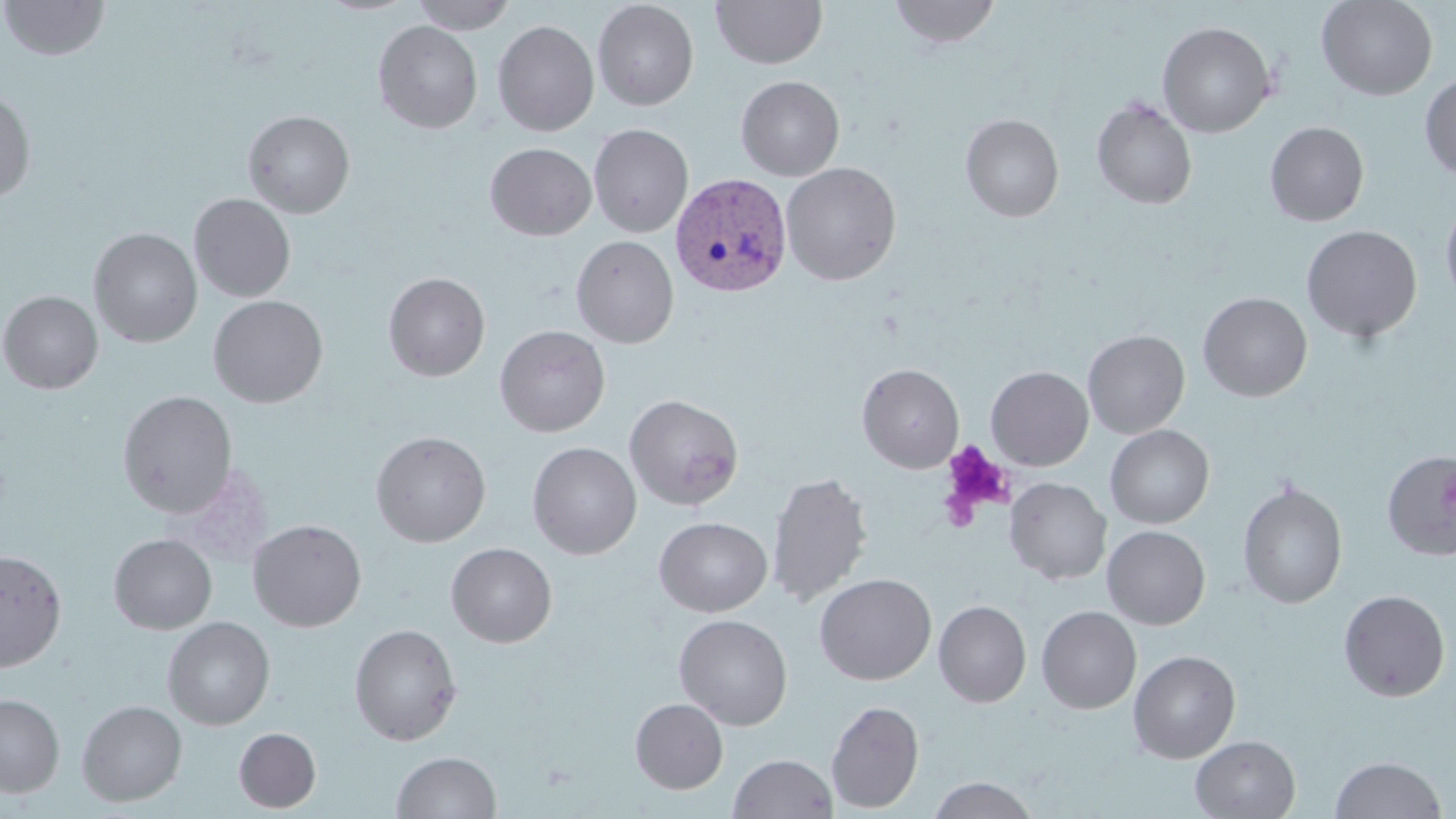
{
  "slide_level_diagnosis": "Plasmodium vivax",
  "magnification": "1000x",
  "uninfected_red_blood_cell_locations": "approximate bounding boxes as (x1,y1)-(x2,y2) corner pairs in pixels: (2,0)-(109,61), (409,0)-(517,34), (711,0)-(827,69), (888,0)-(1002,49), (1317,0)-(1437,100), (592,1)-(699,110), (492,20)-(599,136), (373,21)-(483,133), (1157,21)-(1275,137), (1419,73)-(1456,180), (736,75)-(845,181), (0,90)-(36,203), (1092,96)-(1197,210), (243,110)-(355,218), (960,113)-(1064,222), (1265,121)-(1369,226), (589,124)-(693,237), (485,142)-(597,241), (781,162)-(902,286), (189,193)-(296,302), (1440,195)-(1456,312), (1301,224)-(1422,343), (88,228)-(202,347), (571,235)-(678,348), (383,272)-(490,381), (0,290)-(103,394), (1197,292)-(1312,401), (208,295)-(328,408), (494,324)-(611,437), (1082,329)-(1190,438), (857,363)-(963,473), (986,366)-(1093,470), (117,390)-(238,518), (624,393)-(744,510), (1105,424)-(1214,528), (371,430)-(491,547), (527,441)-(642,559), (1382,450)-(1456,560), (767,470)-(874,607), (1004,477)-(1111,584), (1238,480)-(1347,609), (654,516)-(772,617), (248,519)-(367,632), (1102,525)-(1210,629), (108,533)-(217,633), (446,542)-(557,647), (0,549)-(67,671), (814,573)-(936,685), (1338,589)-(1451,702), (933,600)-(1031,708), (1036,605)-(1142,714), (674,613)-(793,730), (162,616)-(275,730), (348,623)-(462,746), (1128,650)-(1241,763), (0,693)-(65,797), (630,698)-(729,793), (76,699)-(187,806), (825,699)-(924,813), (233,726)-(321,812), (1190,735)-(1300,818), (391,751)-(501,818), (729,753)-(837,819), (1330,755)-(1448,818), (928,776)-(1038,819)",
  "image_size": "1456×819 pixels",
  "preparation": "thin blood film",
  "platelet_locations": "approximate bounding boxes as (x1,y1)-(x2,y2) corner pairs in pixels: (941,442)-(1013,518), (938,486)-(981,533)",
  "plasmodium_vivax_infected_red_blood_cell_locations": "approximate bounding boxes as (x1,y1)-(x2,y2) corner pairs in pixels: (670,172)-(793,297)",
  "field_of_view": "single",
  "modality": "light microscopy",
  "stain": "May-Grünwald-Giemsa"
}